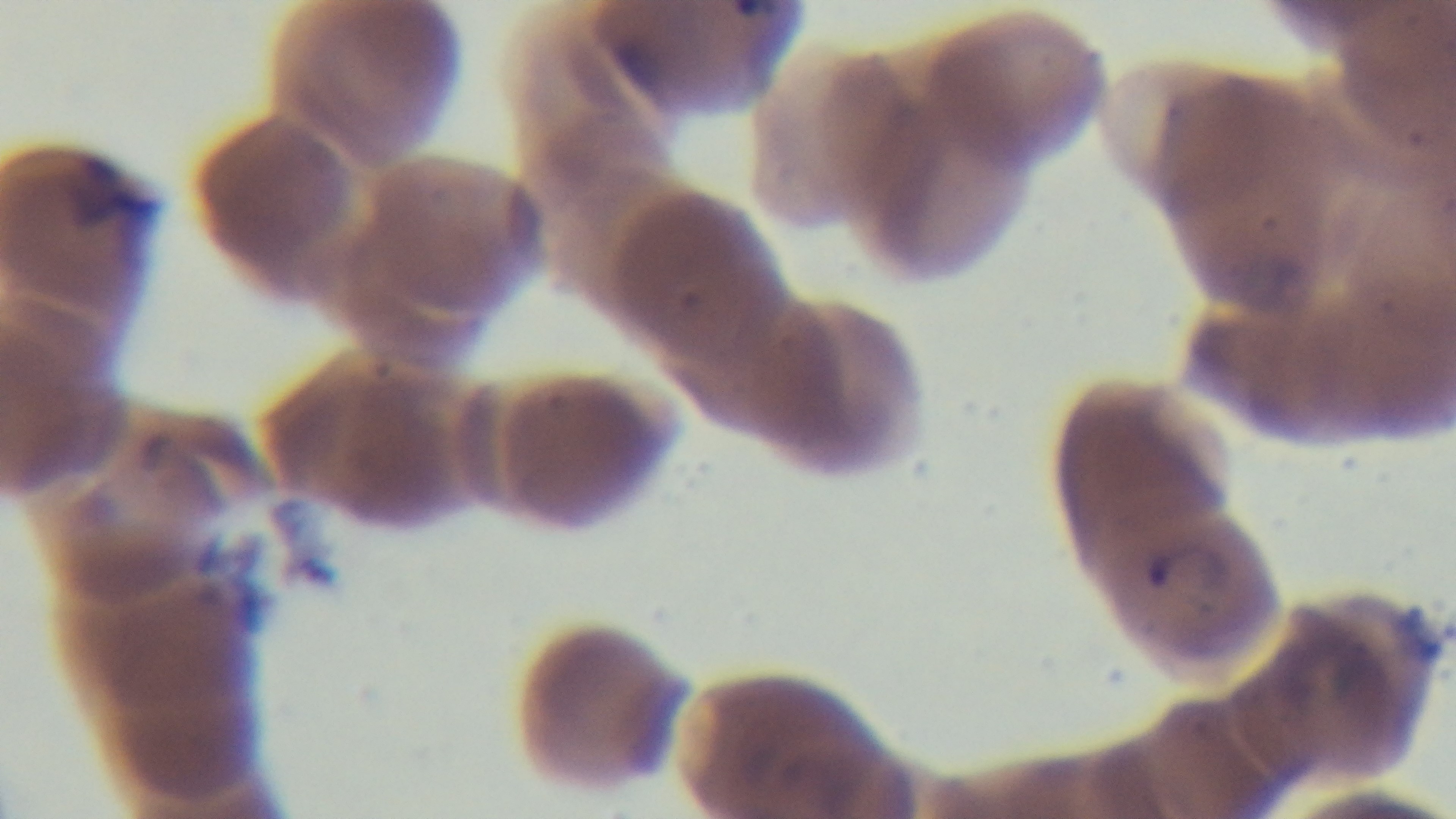
Preparation: thin blood film. Single field of view. Captured with a mounted 4K digital camera. Giemsa-stained. Malaria status: infected. 100x oil-immersion objective. Photomicrograph.